Assess this cell for malaria.
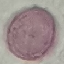
Uninfected.

preparation = thin blood film
stain = Giemsa
image type = cell patch, automatically extracted from a larger field of view and resized to 64 × 64 pixels
capture = smartphone camera at the microscope eyepiece